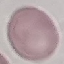 Result: negative for malaria parasites. Thin blood smear. Cell patch, automatically extracted from a larger field of view and resized to 64 × 64 pixels. Giemsa-stained preparation. Photographed with a smartphone camera at the microscope eyepiece.